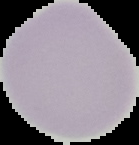 Segmented cell region on a black background. Malaria status: uninfected. Image is 139×145 pixels. From a thin blood smear.